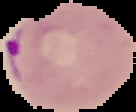
Summary:
  - Image type: segmented cell region with the area outside set to black
  - Result: Plasmodium parasites detected
  - Preparation: thin blood smear
  - Image size: 136×112 pixels